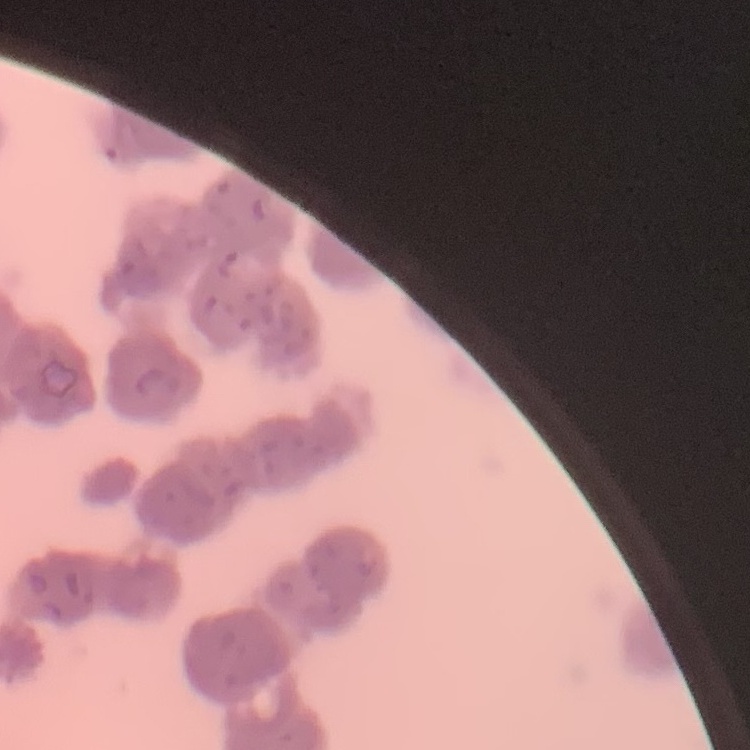
{
  "red_blood_cell_morphology": "rouleaux formation",
  "image_type": "one tile cut from a larger photomicrograph",
  "preparation": "thin peripheral smear",
  "stain": "Field's or Giemsa"
}